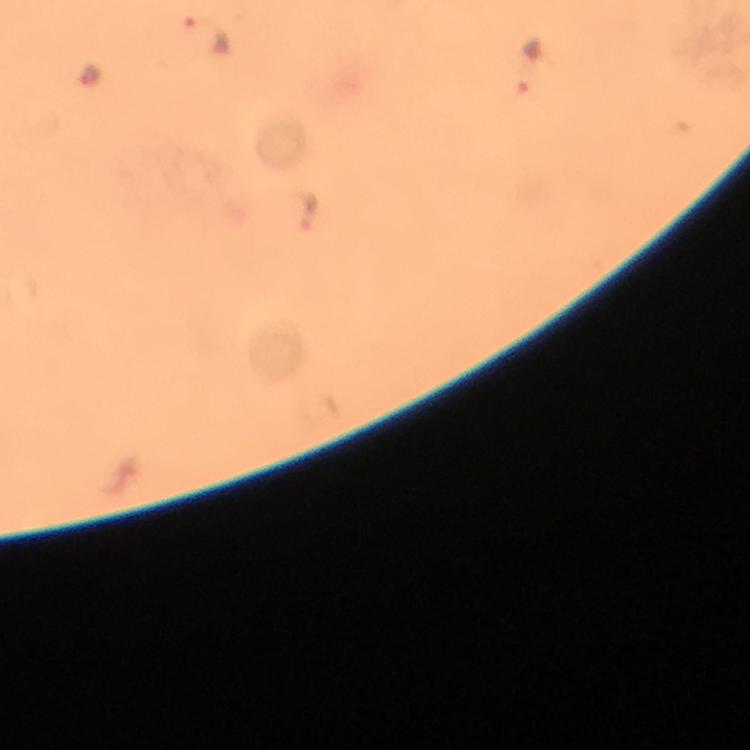
Approximate centers as (x, y) in pixels. Malaria parasite locations: (204, 33), (529, 63), (90, 74), (306, 209). Image is 750×750 pixels. Thick blood film. Immersion oil applied. Photographed with a smartphone mounted on the microscope. Giemsa stain. A crop from one field of view. 100x magnification. From a diagnostic examination for malaria.